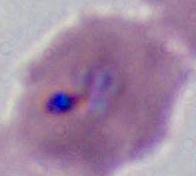

Summary:
  - Identification: Plasmodium
  - Modality: photomicrograph
  - Magnification: 400x or 1000x